Report the malaria status of this cell.
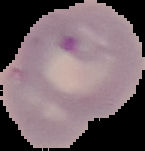
Parasitized.

image size = 145×151 pixels
image type = segmented cell region with the area outside set to black
preparation = thin blood film